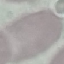

Malaria status: uninfected. Photographed with a smartphone camera at the microscope eyepiece. Giemsa stain. Automatically extracted cell patch, resized to 64 × 64 pixels. Thin smear of blood.